Identify the parasite.
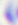

This is Toxoplasma gondii.

magnification = 400x
modality = photomicrograph